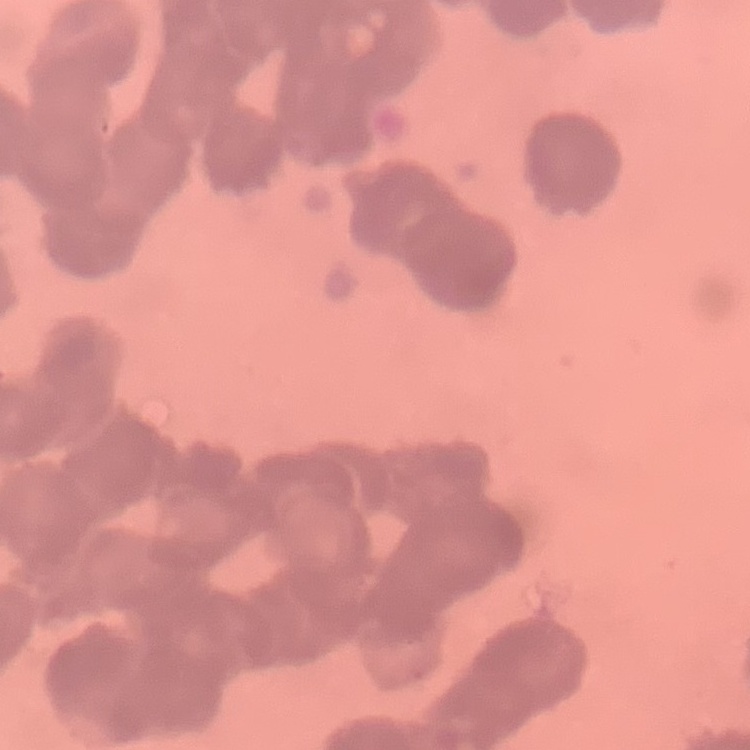
red blood cell morphology = rouleaux formation
image type = one tile cut from a larger photomicrograph
stain = Field's or Giemsa
preparation = thin peripheral smear